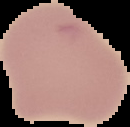
image size = 130×127 pixels
image type = cell region segmented out of the field of view; surrounding area masked to black
preparation = thin blood smear
result = no malaria parasites detected